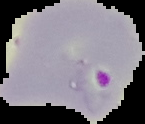

malaria status = parasitized
image type = cell region segmented out of the field of view; surrounding area masked to black
image size = 145×124 pixels
preparation = thin blood smear